State which malaria species this is.
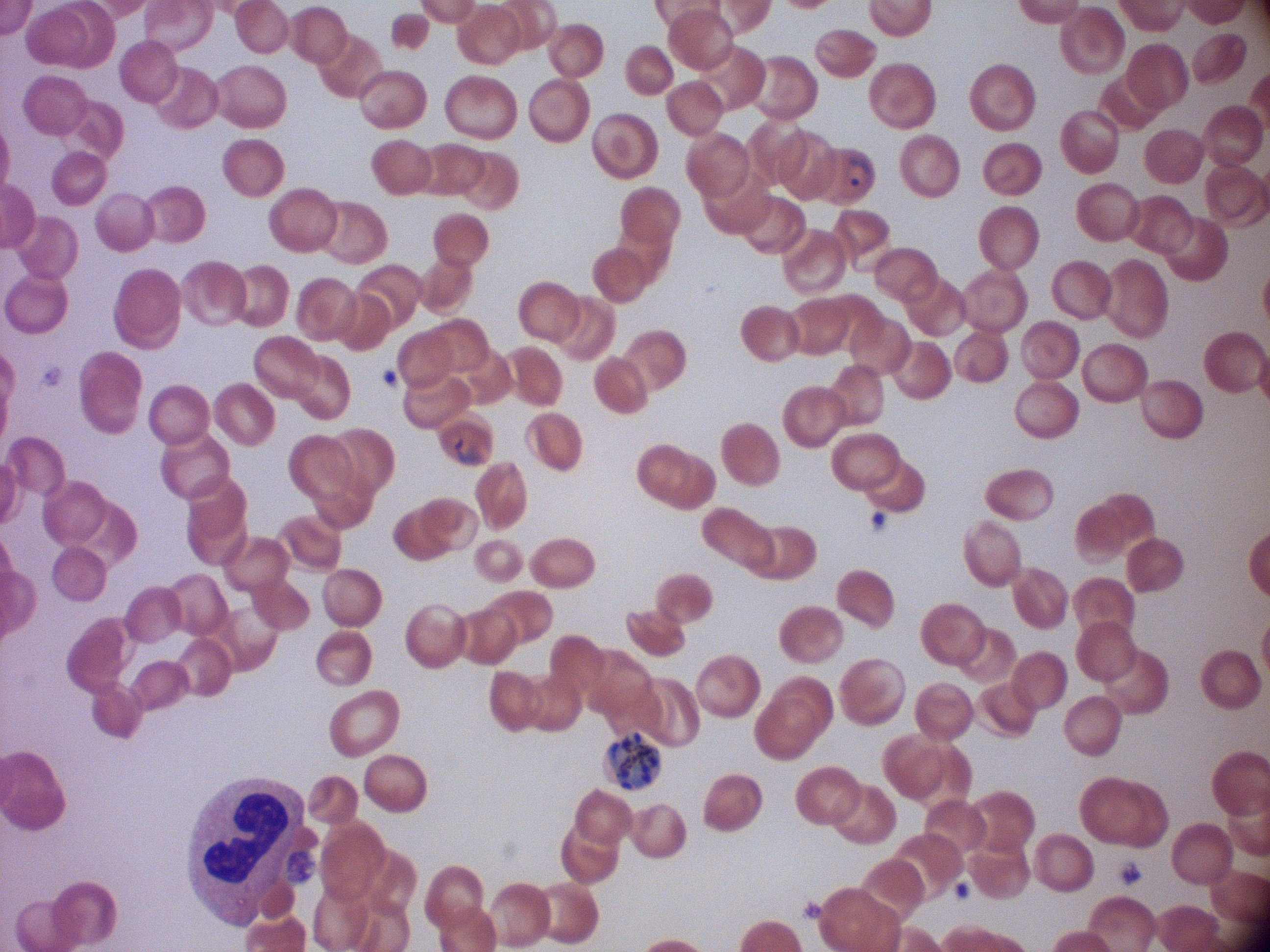
Plasmodium falciparum.

life-cycle stages among the annotated parasites = ring form, schizont
image size = 1270×952 pixels
field of view = single
microscope = Leica DM2000 with built-in camera
ring form locations = approximate bounding boxes as (x1, y1, x2, y2) in pixels, from the source annotation, which is not necessarily exhaustive: (841, 151, 876, 192), (450, 434, 487, 467)
magnification = 100x
schizont locations = approximate bounding boxes as (x1, y1, x2, y2) in pixels, from the source annotation, which is not necessarily exhaustive: (610, 733, 662, 788)
preparation = thin blood film
stain = Giemsa